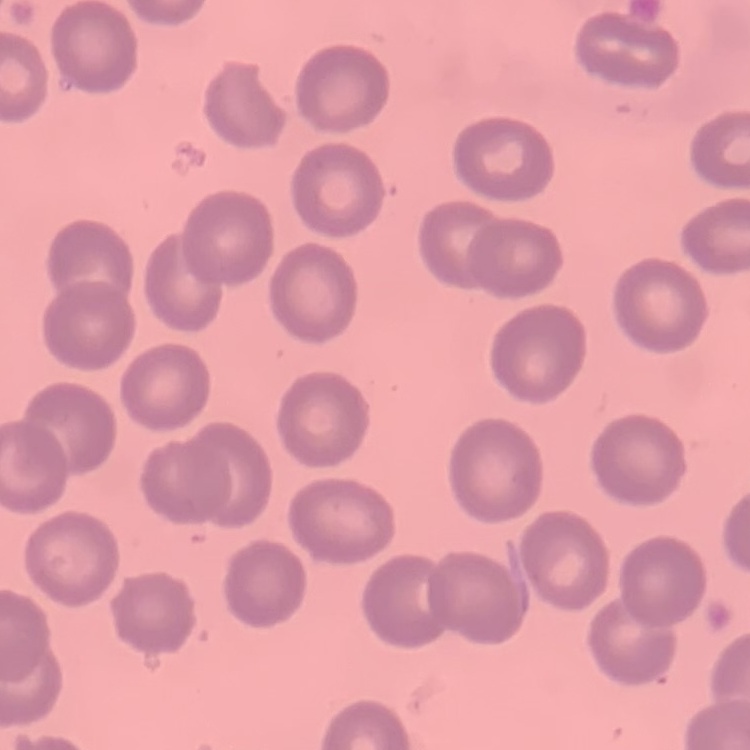
erythrocyte_morphology: no rouleaux formation
stain: Field's or Giemsa
preparation: thin peripheral smear
image_type: square crop of a larger photomicrograph